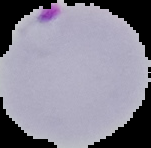

image type = segmented cell region on a black background
preparation = thin blood film
malaria status = parasitized
image size = 151×148 pixels